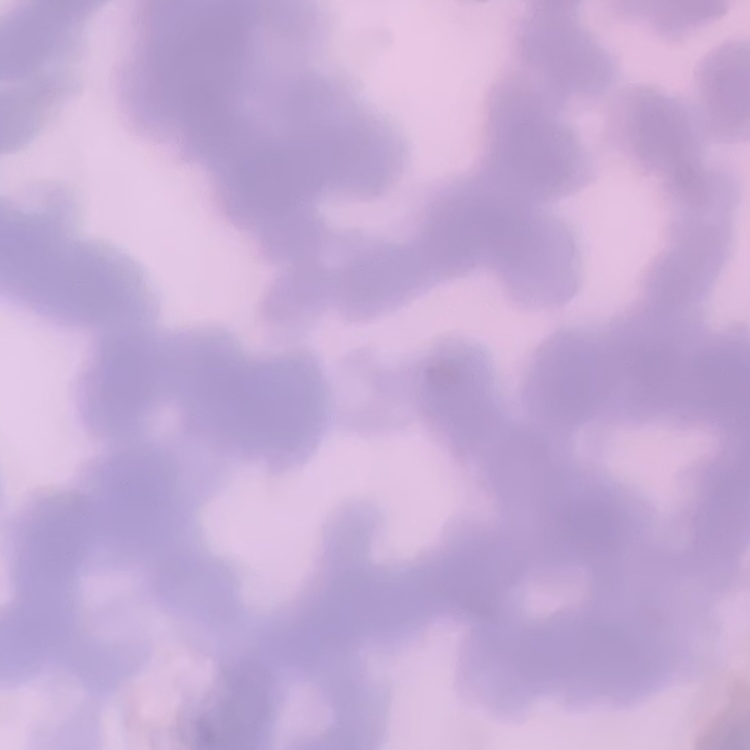

Summary:
  - Red blood cell morphology: rouleaux formation
  - Image type: square crop of a larger photomicrograph
  - Preparation: thin blood smear
  - Stain: Field's or Giemsa